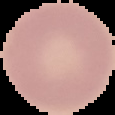

From a thin blood smear. Image is 115×115 pixels. Result: negative for Plasmodium parasites. Cell region segmented out of the field of view; the surrounding area is masked to black.